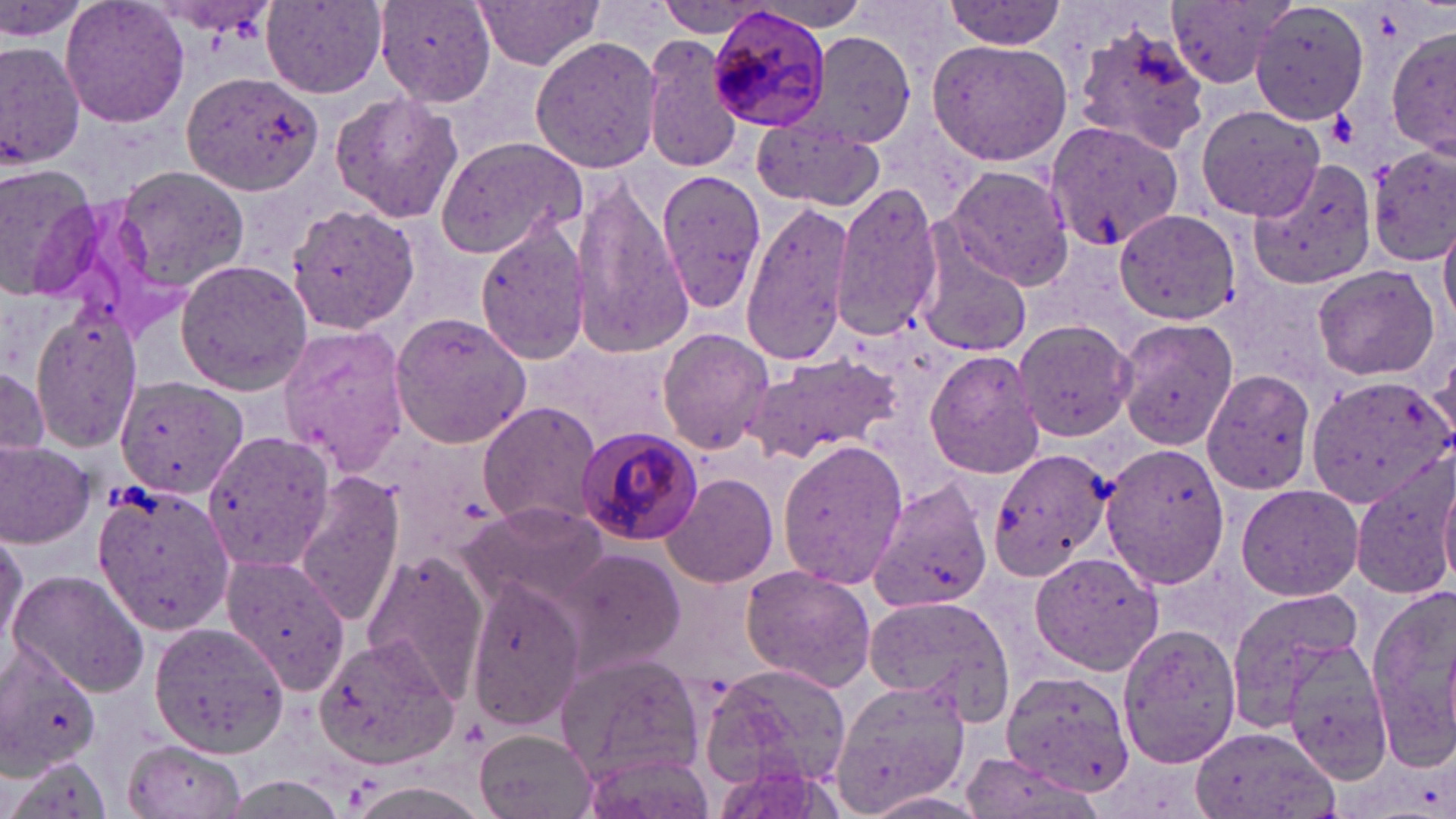
Summary:
  - Coordinate format: approximate bounding boxes as named x1/y1/x2/y2 corners in pixels
  - Platelet locations: (x1=1325, y1=104, x2=1359, y2=150)
  - Plasmodium malariae-infected red blood cell locations: (x1=709, y1=12, x2=832, y2=132), (x1=574, y1=426, x2=701, y2=545)
  - Uninfected red blood cell locations: (x1=2, y1=0, x2=89, y2=43), (x1=61, y1=0, x2=190, y2=130), (x1=376, y1=0, x2=495, y2=107), (x1=940, y1=0, x2=1069, y2=50), (x1=1250, y1=0, x2=1378, y2=123), (x1=471, y1=1, x2=606, y2=71), (x1=1166, y1=1, x2=1293, y2=89), (x1=261, y1=2, x2=387, y2=97), (x1=652, y1=2, x2=775, y2=37), (x1=1069, y1=21, x2=1215, y2=155), (x1=1386, y1=28, x2=1456, y2=156), (x1=808, y1=33, x2=917, y2=147), (x1=530, y1=34, x2=662, y2=176), (x1=0, y1=38, x2=85, y2=172), (x1=644, y1=39, x2=746, y2=174), (x1=927, y1=39, x2=1072, y2=164), (x1=181, y1=73, x2=325, y2=196), (x1=328, y1=91, x2=464, y2=223), (x1=1195, y1=102, x2=1327, y2=222), (x1=751, y1=115, x2=887, y2=211), (x1=1044, y1=119, x2=1184, y2=252), (x1=435, y1=135, x2=588, y2=259), (x1=1369, y1=147, x2=1456, y2=263), (x1=1241, y1=157, x2=1377, y2=290), (x1=1, y1=163, x2=105, y2=299), (x1=111, y1=164, x2=251, y2=295), (x1=649, y1=164, x2=764, y2=319), (x1=942, y1=167, x2=1074, y2=288), (x1=567, y1=172, x2=693, y2=360), (x1=830, y1=183, x2=951, y2=342), (x1=738, y1=201, x2=855, y2=368), (x1=287, y1=203, x2=417, y2=335), (x1=1116, y1=208, x2=1243, y2=325), (x1=474, y1=215, x2=593, y2=366), (x1=1439, y1=217, x2=1456, y2=330), (x1=916, y1=243, x2=1033, y2=358), (x1=174, y1=259, x2=313, y2=394), (x1=1311, y1=263, x2=1441, y2=382), (x1=27, y1=309, x2=145, y2=449), (x1=389, y1=312, x2=532, y2=448), (x1=1115, y1=317, x2=1238, y2=449), (x1=1014, y1=321, x2=1138, y2=442), (x1=277, y1=323, x2=409, y2=473), (x1=656, y1=328, x2=773, y2=454), (x1=925, y1=348, x2=1047, y2=479), (x1=746, y1=353, x2=901, y2=466), (x1=0, y1=365, x2=47, y2=467), (x1=1200, y1=368, x2=1319, y2=497), (x1=113, y1=375, x2=251, y2=501), (x1=1303, y1=376, x2=1451, y2=507), (x1=478, y1=400, x2=603, y2=529), (x1=199, y1=429, x2=332, y2=572), (x1=776, y1=438, x2=911, y2=589), (x1=0, y1=440, x2=95, y2=548), (x1=1100, y1=442, x2=1231, y2=588), (x1=989, y1=448, x2=1113, y2=584), (x1=1348, y1=460, x2=1456, y2=603), (x1=1437, y1=465, x2=1456, y2=590), (x1=662, y1=471, x2=778, y2=588), (x1=294, y1=472, x2=406, y2=626), (x1=866, y1=478, x2=991, y2=614), (x1=91, y1=479, x2=233, y2=635), (x1=1235, y1=482, x2=1363, y2=601), (x1=462, y1=504, x2=608, y2=609), (x1=0, y1=531, x2=25, y2=659), (x1=553, y1=545, x2=685, y2=684), (x1=1030, y1=551, x2=1165, y2=674), (x1=220, y1=553, x2=351, y2=692), (x1=467, y1=553, x2=591, y2=732), (x1=361, y1=556, x2=486, y2=695), (x1=738, y1=564, x2=878, y2=691), (x1=7, y1=569, x2=149, y2=695), (x1=1366, y1=581, x2=1456, y2=760), (x1=1225, y1=586, x2=1370, y2=737), (x1=860, y1=597, x2=1014, y2=709), (x1=149, y1=621, x2=294, y2=759), (x1=1115, y1=623, x2=1242, y2=770), (x1=314, y1=633, x2=457, y2=768), (x1=0, y1=640, x2=100, y2=771), (x1=1278, y1=640, x2=1396, y2=781), (x1=555, y1=652, x2=704, y2=784), (x1=701, y1=657, x2=848, y2=797), (x1=1000, y1=670, x2=1136, y2=793), (x1=829, y1=677, x2=970, y2=815), (x1=1187, y1=725, x2=1335, y2=819), (x1=474, y1=729, x2=598, y2=819), (x1=120, y1=739, x2=247, y2=819), (x1=575, y1=749, x2=711, y2=819), (x1=958, y1=750, x2=1105, y2=819), (x1=2, y1=754, x2=115, y2=819)
  - Slide-level diagnosis: Plasmodium malariae
  - Field of view: one of a larger specimen
  - Image size: 1456×819 pixels
  - Preparation: thin blood film
  - Modality: optical microscopy
  - Stain: May-Grünwald-Giemsa
  - Magnification: 1000x